Locate every blood parasite and identify its species.
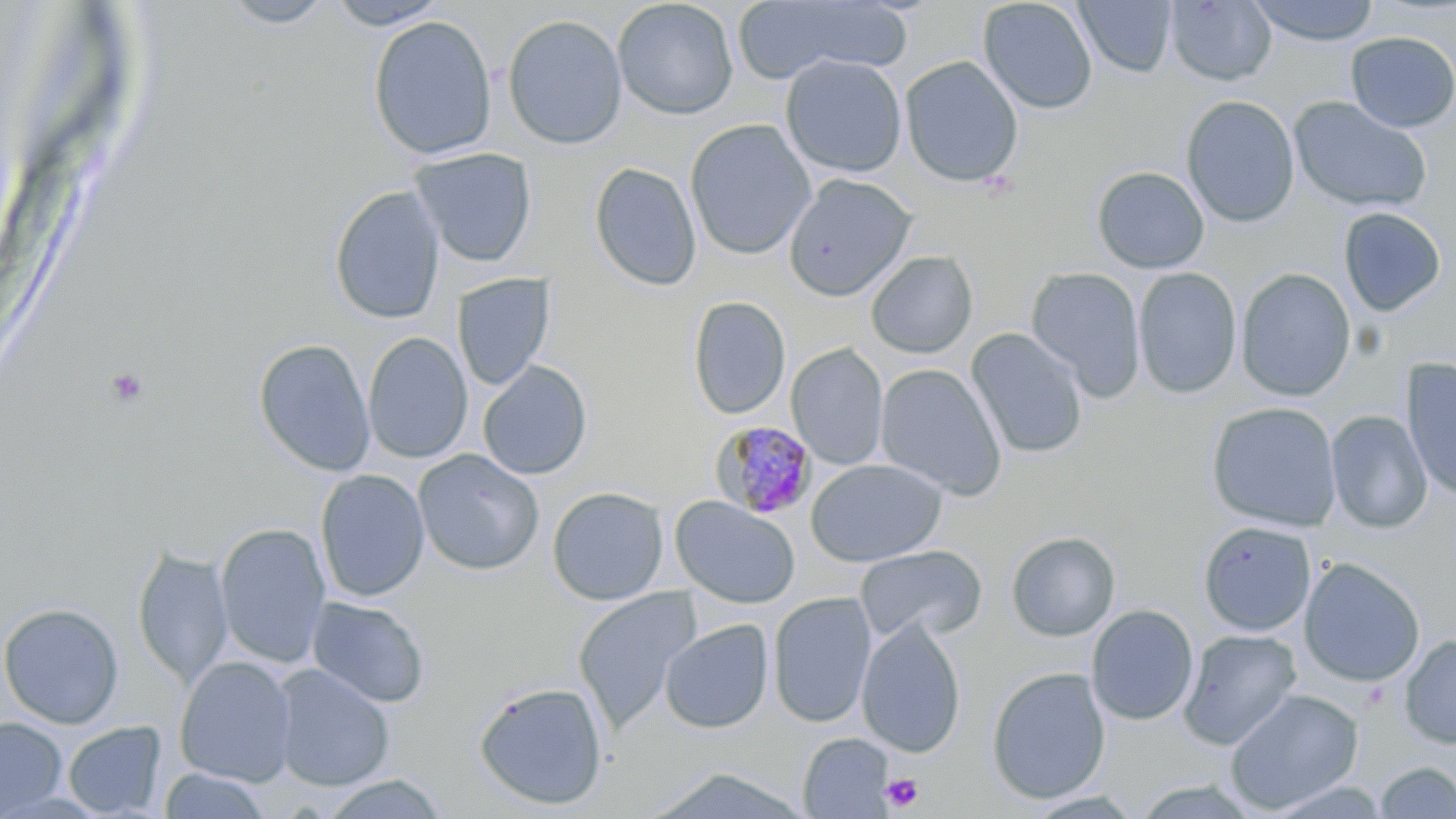
Approximate bounding boxes as [x1, y1, x2, y2] in pixels.
Plasmodium malariae-infected red blood cells: [710, 421, 818, 521].
No Plasmodium falciparum, Plasmodium ovale, Plasmodium vivax, Babesia divergens, or Trypanosoma brucei observed.

slide-level diagnosis = Plasmodium malariae
uninfected red blood cell locations = approximate bounding boxes as [x1, y1, x2, y2] in pixels: [325, 0, 451, 30], [612, 0, 739, 120], [730, 0, 911, 83], [978, 0, 1098, 115], [1246, 0, 1382, 46], [219, 1, 337, 29], [1075, 1, 1178, 78], [1165, 1, 1277, 86], [502, 13, 628, 150], [368, 15, 497, 160], [1345, 31, 1456, 133], [781, 54, 907, 177], [900, 55, 1023, 188], [1180, 95, 1300, 228], [1289, 96, 1432, 214], [685, 118, 816, 260], [409, 147, 537, 268], [589, 162, 702, 291], [1092, 166, 1209, 273], [783, 173, 917, 302], [329, 185, 446, 324], [1338, 207, 1447, 317], [866, 251, 978, 358], [1026, 266, 1146, 400], [1133, 267, 1242, 398], [1236, 267, 1356, 401], [452, 273, 555, 391], [688, 295, 791, 420], [966, 328, 1089, 459], [363, 332, 472, 464], [253, 338, 376, 477], [787, 344, 890, 470], [1400, 357, 1456, 502], [477, 360, 593, 480], [875, 363, 1007, 500], [1206, 401, 1342, 531], [1325, 410, 1433, 534], [413, 449, 544, 575], [806, 458, 948, 567], [315, 469, 430, 602], [547, 486, 669, 606], [670, 496, 800, 609], [1198, 521, 1317, 637], [215, 522, 331, 669], [1006, 531, 1120, 641], [855, 544, 987, 644], [133, 546, 233, 689], [1298, 557, 1425, 688], [572, 587, 703, 734], [768, 592, 877, 728], [306, 596, 431, 708], [0, 602, 124, 729], [1086, 604, 1199, 726], [857, 617, 967, 758], [660, 619, 774, 734], [1177, 629, 1302, 750], [1399, 633, 1456, 749], [174, 656, 297, 787], [272, 664, 395, 791], [987, 667, 1111, 804], [473, 681, 608, 810], [1224, 688, 1364, 814], [0, 716, 67, 817], [63, 721, 167, 817], [798, 733, 894, 818], [1375, 761, 1456, 818], [159, 767, 272, 819], [645, 767, 815, 819], [318, 774, 449, 818]
platelet locations = approximate bounding boxes as [x1, y1, x2, y2] in pixels: [106, 368, 149, 406], [882, 773, 924, 812]
preparation = thin blood smear
image size = 1456×819 pixels
field of view = single
magnification = 1000x
modality = light microscopy
stain = May-Grünwald-Giemsa